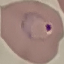
Summary:
  - Result: malaria parasites identified
  - Preparation: thin blood smear
  - Stain: Giemsa
  - Image type: automatically extracted cell patch, resized to 64 × 64 pixels
  - Capture: smartphone camera at the microscope eyepiece